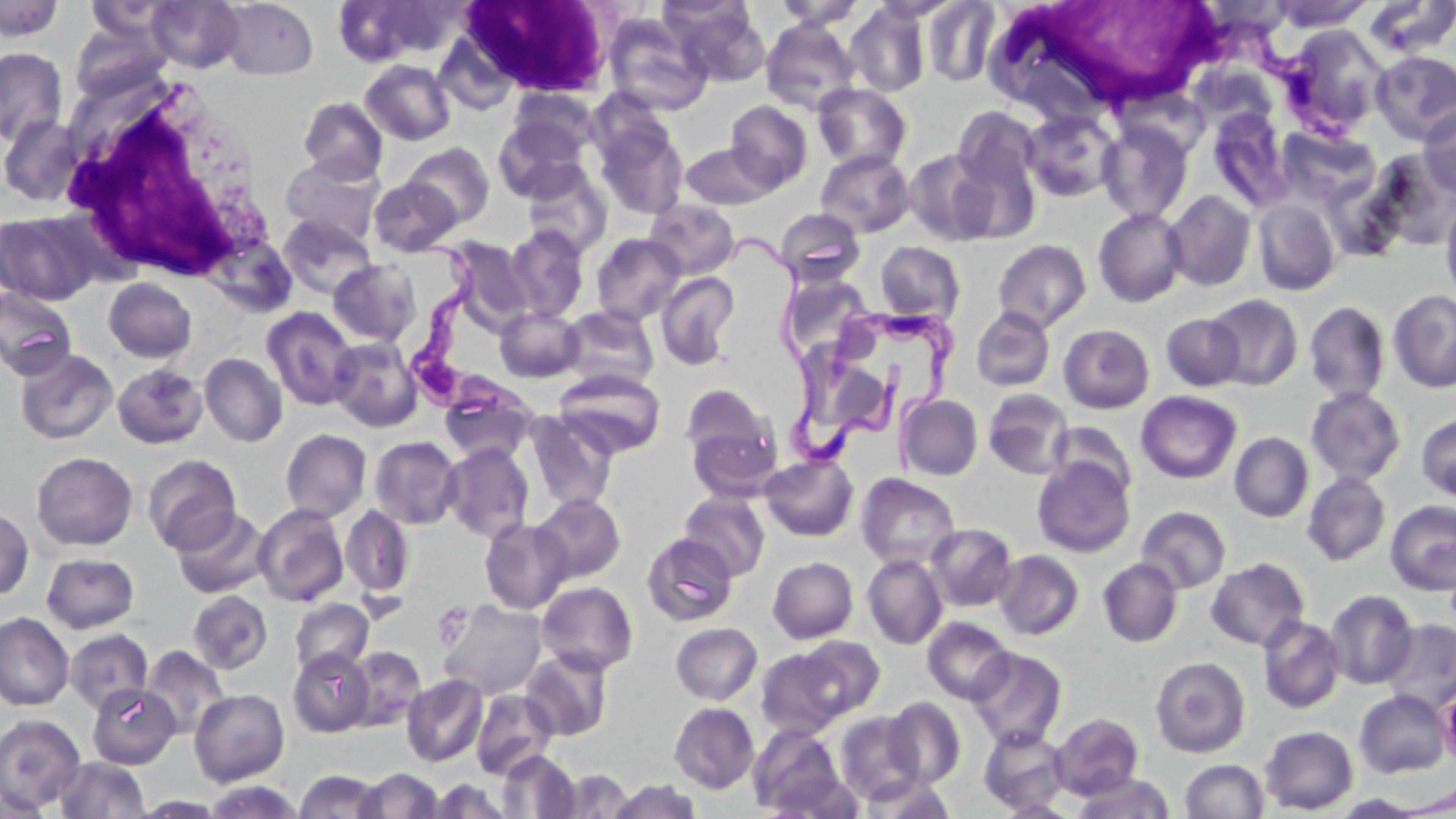
Summary:
  - Coordinate format: approximate bounding boxes as named x1/y1/x2/y2 corners in pixels
  - White blood cell locations: (x1=460, y1=0, x2=615, y2=95), (x1=1014, y1=0, x2=1240, y2=107), (x1=53, y1=78, x2=275, y2=288)
  - Platelet locations: (x1=433, y1=602, x2=473, y2=648)
  - Trypanosoma brucei locations: (x1=398, y1=230, x2=534, y2=424), (x1=732, y1=235, x2=901, y2=470), (x1=827, y1=301, x2=959, y2=430)
  - Uninfected red blood cell locations: (x1=146, y1=0, x2=245, y2=73), (x1=219, y1=0, x2=318, y2=79), (x1=773, y1=0, x2=865, y2=29), (x1=1272, y1=0, x2=1374, y2=32), (x1=0, y1=1, x2=63, y2=41), (x1=85, y1=1, x2=179, y2=42), (x1=922, y1=1, x2=1000, y2=86), (x1=1362, y1=1, x2=1456, y2=57), (x1=332, y1=2, x2=431, y2=67), (x1=845, y1=2, x2=932, y2=98), (x1=668, y1=3, x2=770, y2=87), (x1=603, y1=14, x2=711, y2=116), (x1=70, y1=20, x2=168, y2=101), (x1=761, y1=20, x2=861, y2=114), (x1=1281, y1=25, x2=1389, y2=136), (x1=435, y1=36, x2=518, y2=116), (x1=0, y1=48, x2=68, y2=145), (x1=1371, y1=51, x2=1456, y2=144), (x1=360, y1=59, x2=455, y2=145), (x1=813, y1=83, x2=912, y2=171), (x1=509, y1=89, x2=597, y2=156), (x1=298, y1=96, x2=388, y2=183), (x1=725, y1=100, x2=813, y2=192), (x1=1418, y1=104, x2=1456, y2=197), (x1=952, y1=107, x2=1042, y2=197), (x1=1022, y1=108, x2=1121, y2=203), (x1=1207, y1=108, x2=1293, y2=211), (x1=493, y1=114, x2=591, y2=202), (x1=1, y1=115, x2=83, y2=207), (x1=594, y1=120, x2=688, y2=219), (x1=1097, y1=121, x2=1193, y2=223), (x1=1276, y1=127, x2=1378, y2=207), (x1=681, y1=142, x2=777, y2=209), (x1=402, y1=143, x2=494, y2=226), (x1=905, y1=148, x2=1003, y2=246), (x1=815, y1=149, x2=915, y2=237), (x1=1372, y1=149, x2=1456, y2=250), (x1=281, y1=155, x2=386, y2=245), (x1=521, y1=164, x2=612, y2=259), (x1=1320, y1=173, x2=1408, y2=262), (x1=369, y1=177, x2=462, y2=256), (x1=1163, y1=190, x2=1257, y2=291), (x1=644, y1=199, x2=741, y2=279), (x1=1253, y1=199, x2=1341, y2=295), (x1=1440, y1=199, x2=1456, y2=305), (x1=775, y1=208, x2=866, y2=286), (x1=1093, y1=208, x2=1187, y2=307), (x1=1, y1=210, x2=102, y2=306), (x1=278, y1=214, x2=377, y2=300), (x1=505, y1=225, x2=589, y2=321), (x1=591, y1=233, x2=685, y2=326), (x1=447, y1=239, x2=534, y2=335), (x1=993, y1=239, x2=1091, y2=332), (x1=875, y1=241, x2=965, y2=323), (x1=327, y1=259, x2=422, y2=346), (x1=656, y1=272, x2=740, y2=369), (x1=104, y1=277, x2=196, y2=363), (x1=792, y1=278, x2=869, y2=352), (x1=0, y1=288, x2=76, y2=381), (x1=1388, y1=289, x2=1456, y2=393), (x1=1205, y1=294, x2=1303, y2=390), (x1=1303, y1=301, x2=1390, y2=403), (x1=494, y1=306, x2=584, y2=382), (x1=559, y1=306, x2=659, y2=390), (x1=971, y1=306, x2=1055, y2=392), (x1=261, y1=307, x2=359, y2=410), (x1=1161, y1=313, x2=1246, y2=392), (x1=1058, y1=324, x2=1154, y2=414), (x1=329, y1=337, x2=421, y2=431), (x1=806, y1=337, x2=890, y2=430), (x1=15, y1=349, x2=117, y2=444), (x1=199, y1=352, x2=287, y2=447), (x1=112, y1=363, x2=207, y2=449), (x1=555, y1=368, x2=666, y2=458), (x1=438, y1=380, x2=538, y2=465), (x1=680, y1=383, x2=781, y2=491), (x1=1305, y1=386, x2=1406, y2=486), (x1=983, y1=388, x2=1074, y2=479), (x1=1136, y1=391, x2=1241, y2=484), (x1=896, y1=394, x2=983, y2=480), (x1=524, y1=411, x2=619, y2=512), (x1=1416, y1=414, x2=1456, y2=502), (x1=1048, y1=422, x2=1137, y2=498), (x1=280, y1=429, x2=371, y2=521), (x1=1229, y1=432, x2=1313, y2=522), (x1=369, y1=436, x2=463, y2=529), (x1=441, y1=443, x2=534, y2=543), (x1=31, y1=451, x2=138, y2=551), (x1=143, y1=454, x2=242, y2=554), (x1=760, y1=454, x2=858, y2=541), (x1=1032, y1=456, x2=1135, y2=557), (x1=1302, y1=472, x2=1390, y2=566), (x1=856, y1=473, x2=960, y2=570), (x1=678, y1=491, x2=769, y2=581), (x1=532, y1=494, x2=626, y2=583), (x1=1385, y1=500, x2=1456, y2=594), (x1=253, y1=504, x2=348, y2=606), (x1=341, y1=504, x2=414, y2=598), (x1=0, y1=506, x2=34, y2=600), (x1=1136, y1=506, x2=1231, y2=593), (x1=172, y1=507, x2=270, y2=599), (x1=479, y1=518, x2=573, y2=613), (x1=926, y1=523, x2=1017, y2=611), (x1=641, y1=532, x2=738, y2=627), (x1=994, y1=550, x2=1084, y2=640), (x1=41, y1=552, x2=140, y2=634), (x1=862, y1=554, x2=948, y2=649), (x1=767, y1=557, x2=858, y2=644), (x1=1098, y1=557, x2=1183, y2=647), (x1=1206, y1=558, x2=1310, y2=651), (x1=536, y1=581, x2=639, y2=675), (x1=187, y1=590, x2=272, y2=674), (x1=1325, y1=590, x2=1418, y2=689), (x1=290, y1=599, x2=374, y2=675), (x1=438, y1=599, x2=547, y2=699), (x1=0, y1=613, x2=74, y2=710), (x1=1257, y1=615, x2=1346, y2=714), (x1=922, y1=616, x2=1015, y2=705), (x1=1381, y1=618, x2=1456, y2=715), (x1=670, y1=622, x2=763, y2=705), (x1=65, y1=629, x2=153, y2=715), (x1=794, y1=635, x2=885, y2=718), (x1=141, y1=645, x2=230, y2=738), (x1=344, y1=646, x2=425, y2=730), (x1=755, y1=646, x2=854, y2=738), (x1=288, y1=647, x2=375, y2=737), (x1=967, y1=647, x2=1068, y2=748), (x1=521, y1=649, x2=614, y2=741), (x1=1150, y1=655, x2=1251, y2=758), (x1=401, y1=674, x2=487, y2=767), (x1=88, y1=683, x2=180, y2=769), (x1=189, y1=689, x2=289, y2=786), (x1=471, y1=689, x2=557, y2=779), (x1=1354, y1=690, x2=1451, y2=778), (x1=883, y1=697, x2=966, y2=787), (x1=669, y1=702, x2=759, y2=794), (x1=834, y1=711, x2=925, y2=804), (x1=1050, y1=713, x2=1144, y2=799), (x1=0, y1=714, x2=86, y2=814), (x1=748, y1=724, x2=845, y2=815), (x1=978, y1=725, x2=1071, y2=814), (x1=1260, y1=725, x2=1358, y2=814), (x1=497, y1=749, x2=581, y2=818), (x1=54, y1=757, x2=151, y2=818), (x1=1180, y1=760, x2=1269, y2=818), (x1=355, y1=768, x2=444, y2=818), (x1=294, y1=769, x2=386, y2=818), (x1=554, y1=769, x2=634, y2=817), (x1=767, y1=773, x2=866, y2=818), (x1=1074, y1=773, x2=1175, y2=818), (x1=859, y1=774, x2=956, y2=818), (x1=427, y1=778, x2=514, y2=817), (x1=609, y1=778, x2=702, y2=819), (x1=202, y1=780, x2=306, y2=819), (x1=1394, y1=783, x2=1455, y2=816), (x1=1329, y1=794, x2=1431, y2=817), (x1=994, y1=799, x2=1081, y2=817)
  - Slide-level diagnosis: Trypanosoma brucei
  - Preparation: thin blood smear
  - Stain: May-Grünwald-Giemsa
  - Magnification: 1000x
  - Modality: optical microscopy
  - Field of view: one of a larger specimen
  - Image size: 1456×819 pixels